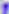

Summary:
  - Identification: Toxoplasma gondii
  - Magnification: 400x
  - Modality: micrograph